Identify the blood parasite species.
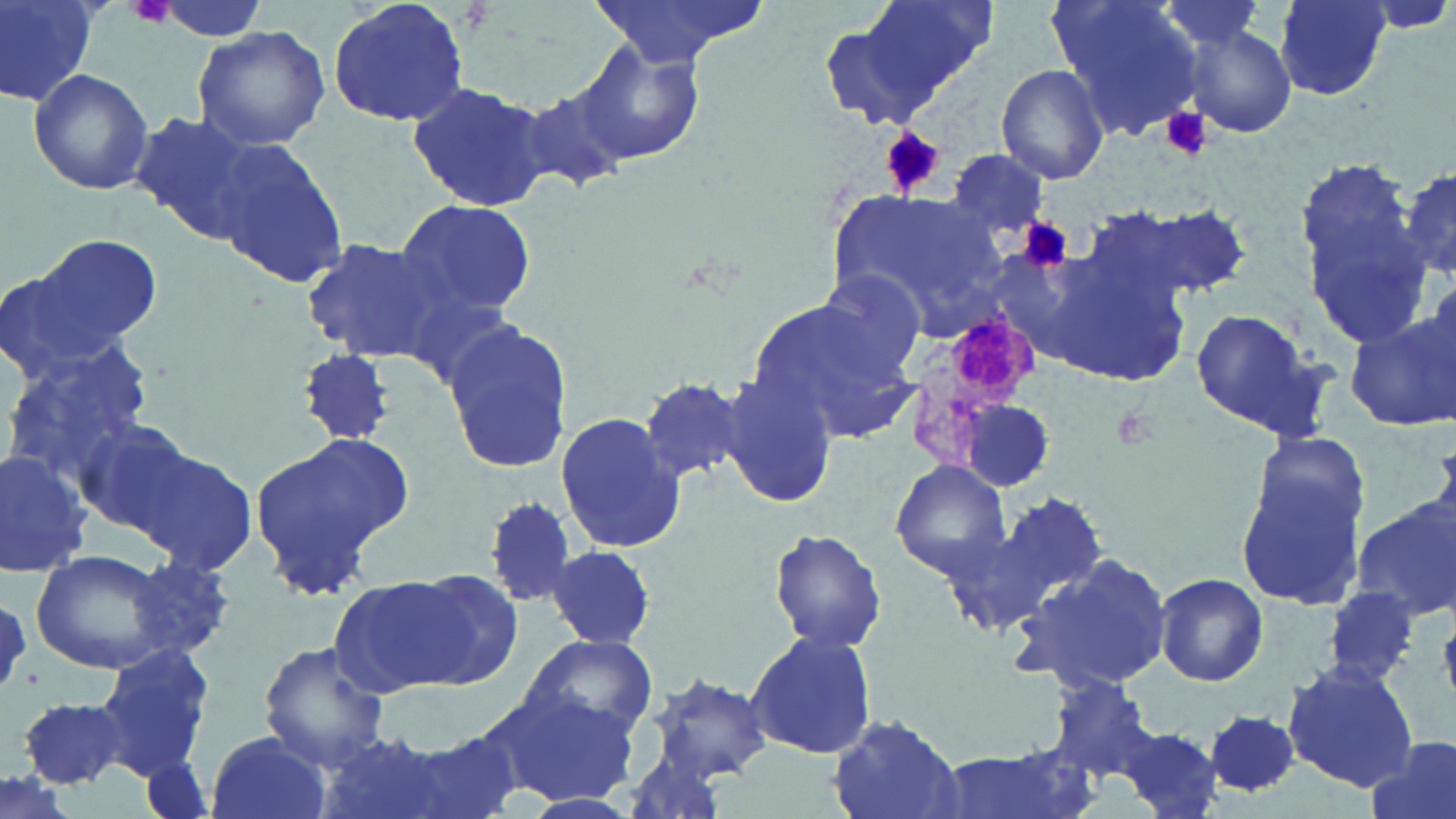
Plasmodium malariae.

modality = optical microscopy
uninfected red blood cell locations = approximate bounding boxes as (x1,y1)-(x2,y2) corner pairs in pixels: (1,0)-(102,106), (327,0)-(471,127), (586,0)-(773,70), (857,0)-(997,99), (1048,0)-(1204,138), (1155,0)-(1273,57), (1278,0)-(1391,99), (1344,0)-(1456,37), (1181,22)-(1297,138), (193,25)-(331,150), (574,43)-(706,167), (994,65)-(1110,186), (28,66)-(153,196), (514,81)-(636,200), (408,82)-(549,212), (130,111)-(275,246), (212,137)-(348,286), (947,149)-(1049,240), (1296,158)-(1431,342), (1399,166)-(1456,283), (825,188)-(1010,327), (395,199)-(537,319), (1116,203)-(1253,300), (21,234)-(163,364), (1025,236)-(1198,389), (300,237)-(453,361), (1420,273)-(1456,381), (746,293)-(914,437), (1188,308)-(1333,440), (1345,310)-(1454,431), (441,319)-(576,475), (298,348)-(394,446), (3,351)-(153,496), (720,372)-(838,509), (639,376)-(748,485), (959,400)-(1055,493), (556,412)-(686,550), (74,419)-(197,534), (251,431)-(413,596), (124,441)-(259,578), (0,446)-(96,576), (890,461)-(1011,580), (1238,474)-(1368,606), (981,492)-(1108,625), (483,496)-(580,610), (1351,501)-(1456,622), (770,528)-(886,654), (547,544)-(657,650), (30,551)-(177,675), (1012,553)-(1176,693), (125,554)-(238,663), (406,570)-(524,684), (329,571)-(501,698), (1154,572)-(1268,686), (1320,587)-(1420,688), (743,630)-(878,759), (522,635)-(659,741), (94,641)-(216,774), (257,644)-(393,772), (1283,661)-(1421,791), (651,673)-(772,784), (1043,679)-(1168,781), (479,685)-(636,804), (829,710)-(965,818), (1205,710)-(1302,798), (1116,727)-(1224,818), (204,729)-(332,819), (312,732)-(454,819), (388,733)-(525,819), (1365,734)-(1456,819), (617,744)-(729,819), (139,750)-(215,819)
field of view = single
stain = May-Grünwald-Giemsa
platelet locations = approximate bounding boxes as (x1,y1)-(x2,y2) corner pairs in pixels: (127,0)-(176,30), (1161,107)-(1211,159), (882,128)-(943,196), (1022,219)-(1069,271), (1023,220)-(1070,269), (1111,405)-(1161,452)
preparation = thin blood film
image size = 1456×819 pixels
Plasmodium malariae-infected red blood cell locations = approximate bounding boxes as (x1,y1)-(x2,y2) corner pairs in pixels: (908,314)-(1040,464)
magnification = 1000x